Classify this cell by malaria status.
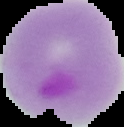

It is parasitized.

Summary:
  - Preparation: thin blood film
  - Image type: segmented cell region with the area outside set to black
  - Image size: 124×127 pixels